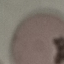

result = no malaria parasites seen
stain = Giemsa
preparation = thin blood smear
image type = automatically extracted cell patch, resized to 64 × 64 pixels
capture = smartphone through the microscope eyepiece